Assess the morphology of the red blood cells.
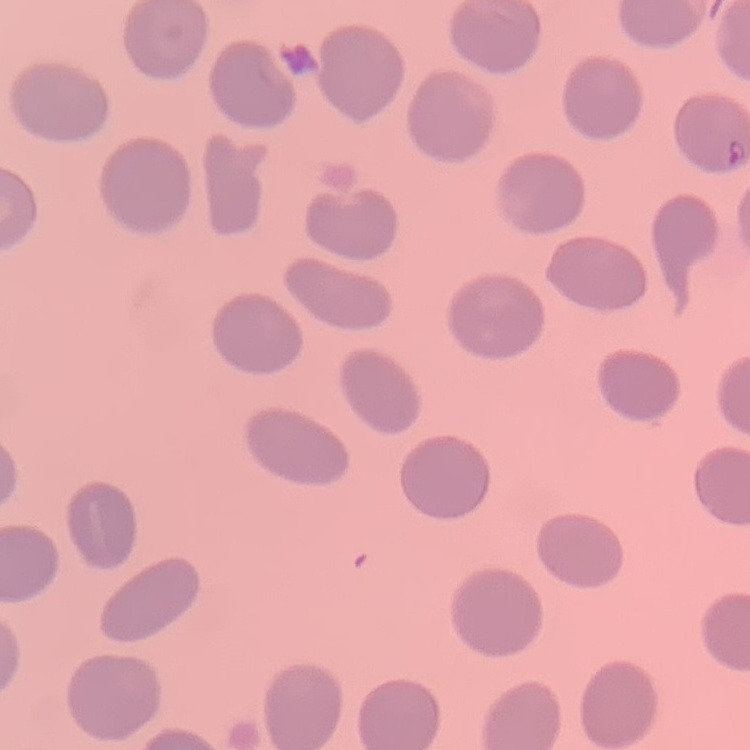

They show no rouleaux formation.

image type = one tile cut from a larger photomicrograph
stain = Field's or Giemsa
preparation = thin peripheral smear